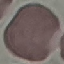

result: no malaria parasites seen
capture: smartphone camera at the microscope eyepiece
stain: Giemsa
image_type: cell patch, automatically extracted from a larger field of view and resized to 64 × 64 pixels
preparation: thin blood film